Name the parasite shown.
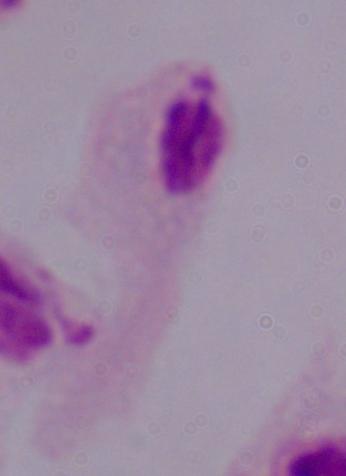

A trichomonad.

1000x magnification. Photomicrograph.